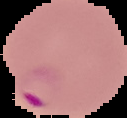

Summary:
  - Result: Plasmodium parasites identified
  - Image type: segmented cell region with the area outside set to black
  - Image size: 127×118 pixels
  - Preparation: thin blood film